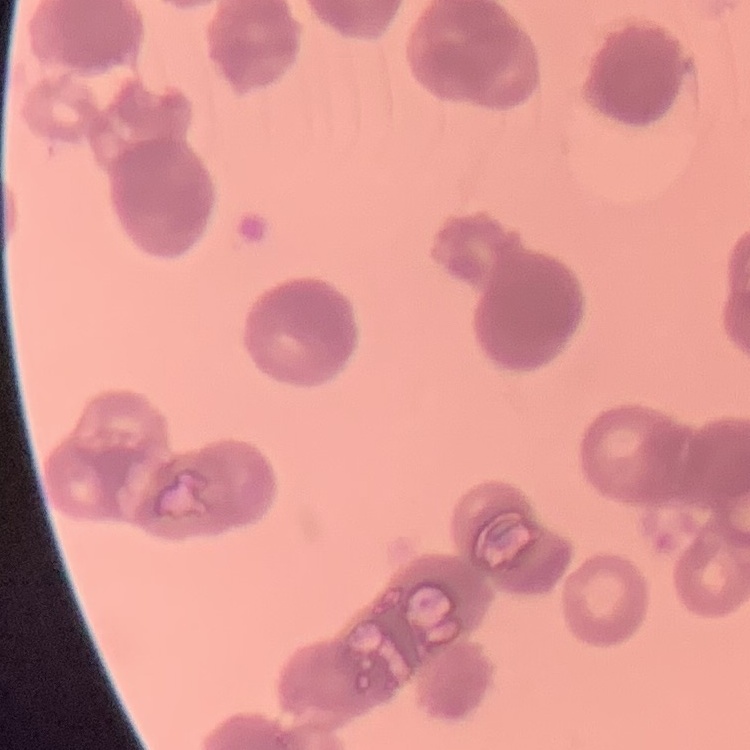
erythrocyte morphology = rouleaux formation
stain = Field's or Giemsa
image type = one tile cut from a larger photomicrograph
preparation = thin blood film